Classify this cell by malaria status.
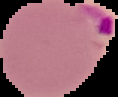
Parasitized.

Summary:
  - Preparation: thin blood film
  - Image size: 118×97 pixels
  - Image type: cell region segmented out of the field of view; surrounding area masked to black